Report the malaria status of this cell.
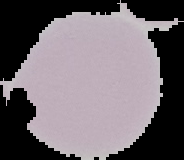

Uninfected.

Summary:
  - Image type: segmented cell region with the area outside set to black
  - Preparation: thin blood film
  - Image size: 184×160 pixels